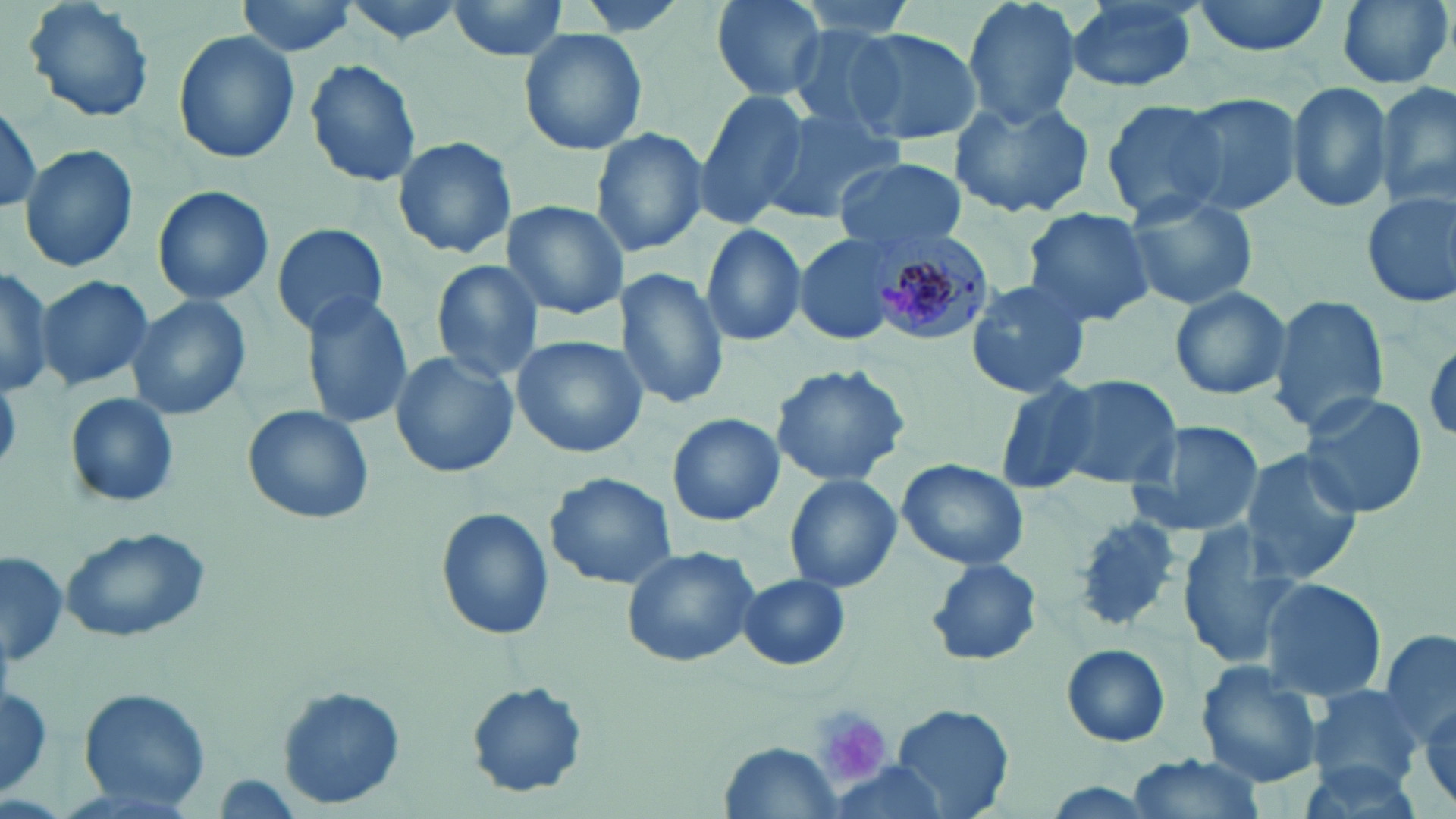
Approximate bounding boxes as (x1,y1)-(x2,y2) corner pairs in pixels. Plasmodium malariae-infected red blood cell locations: (867,224)-(992,343). Uninfected red blood cell locations: (19,0)-(157,125), (234,0)-(362,57), (442,0)-(576,63), (707,0)-(833,102), (791,0)-(922,45), (960,0)-(1085,130), (1190,0)-(1333,58), (1334,0)-(1453,90), (1060,2)-(1202,95), (783,25)-(917,137), (517,26)-(649,158), (842,27)-(983,145), (173,29)-(299,165), (305,58)-(422,186), (1376,80)-(1455,212), (1284,81)-(1393,214), (694,89)-(810,229), (1167,93)-(1302,217), (950,95)-(1098,219), (1098,98)-(1231,221), (1,102)-(44,216), (760,103)-(905,225), (590,127)-(708,256), (392,134)-(517,259), (19,143)-(138,272), (831,158)-(970,253), (152,185)-(275,306), (1359,188)-(1456,309), (1124,191)-(1257,312), (500,200)-(629,319), (1020,207)-(1155,329), (270,222)-(389,335), (699,222)-(807,348), (796,234)-(901,346), (429,259)-(545,383), (0,265)-(54,396), (616,269)-(729,410), (35,275)-(152,391), (963,279)-(1094,398), (1169,286)-(1292,400), (300,293)-(413,429), (1270,294)-(1388,435), (125,295)-(253,422), (511,335)-(648,459), (1425,341)-(1456,441), (388,351)-(518,478), (770,363)-(911,486), (1046,373)-(1182,491), (990,380)-(1103,497), (65,391)-(180,508), (1298,392)-(1428,518), (243,405)-(374,526), (667,413)-(783,527), (1127,418)-(1266,540), (1239,449)-(1364,581), (897,458)-(1029,570), (546,471)-(675,588), (785,473)-(903,595), (436,507)-(554,643), (1072,517)-(1187,635), (1174,522)-(1305,670), (60,527)-(209,642), (620,544)-(761,668), (1,549)-(65,672), (925,558)-(1041,666), (738,573)-(851,670), (1256,577)-(1386,702), (1380,627)-(1456,742), (1061,644)-(1171,747), (1196,662)-(1326,790), (466,683)-(587,797), (0,685)-(52,797), (1308,685)-(1424,787), (278,688)-(403,808), (75,689)-(211,811), (891,705)-(1013,817), (721,742)-(845,815), (1125,753)-(1267,819), (824,762)-(952,815), (1036,781)-(1165,818). Platelet locations: (810,705)-(895,785). Slide-level diagnosis: Plasmodium malariae. 1000x magnification. Image is 1456×819 pixels. Single field of view. Thin blood film. May-Grünwald-Giemsa-stained preparation. Light microscopy.